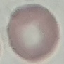
malaria status = uninfected
capture = smartphone camera at the microscope eyepiece
preparation = thin blood film
stain = Giemsa
image type = cell patch, automatically extracted from a larger field of view and resized to 64 × 64 pixels